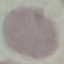
result = no malaria parasites seen
image type = automatically extracted cell patch, resized to 64 × 64 pixels
preparation = thin smear
stain = Giemsa
capture = smartphone camera at the microscope eyepiece